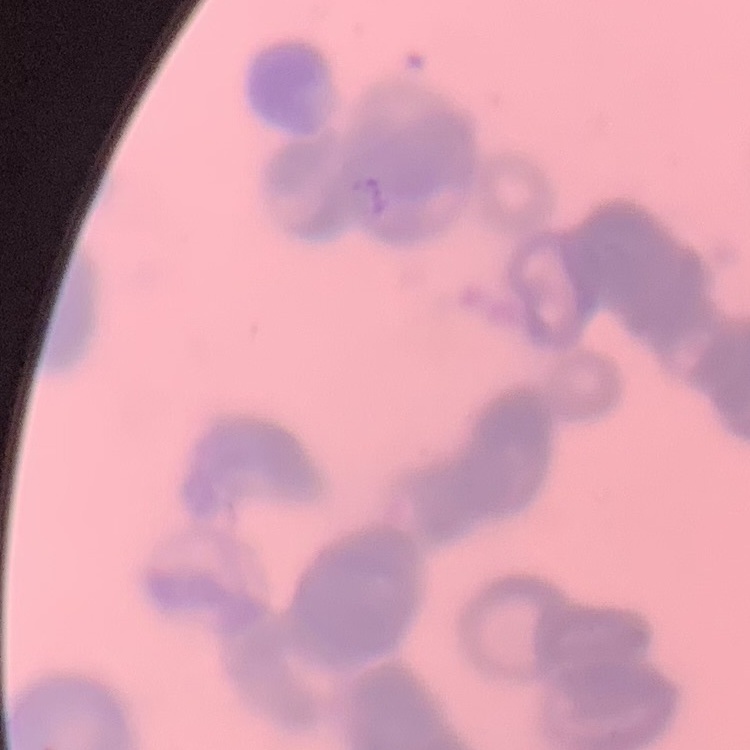

The red blood cells exhibit rouleaux formation. Stained with either Field's or Giemsa. Thin blood smear. One tile cut from a larger photomicrograph.